Describe the morphology of the erythrocytes.
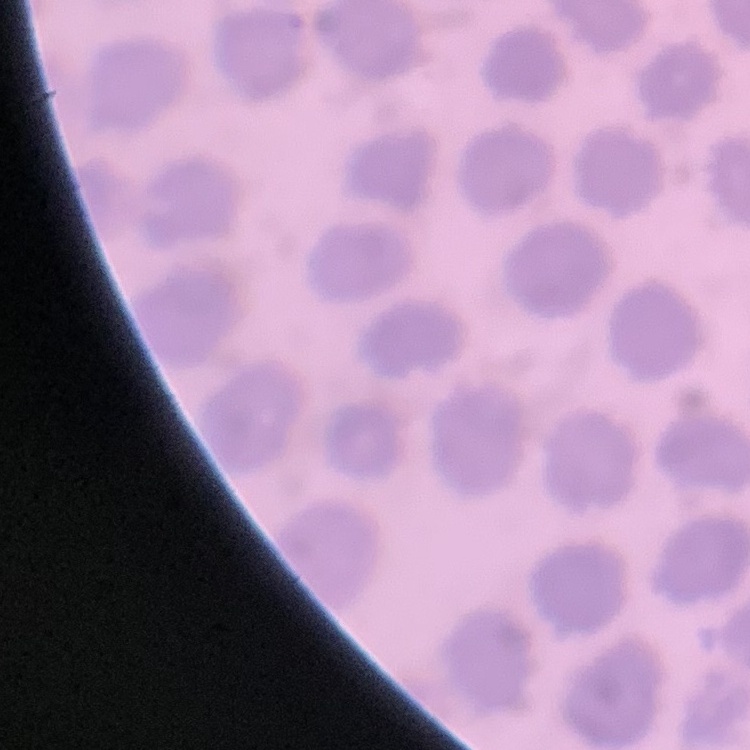
They show no rouleaux formation.

image_type: one tile cut from a larger photomicrograph
stain: Field's or Giemsa
preparation: thin blood film